Classify this cell by malaria status.
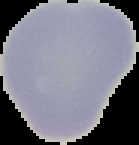
Uninfected.

image size = 139×145 pixels
image type = cell region segmented out of the field of view; surrounding area masked to black
preparation = thin blood film